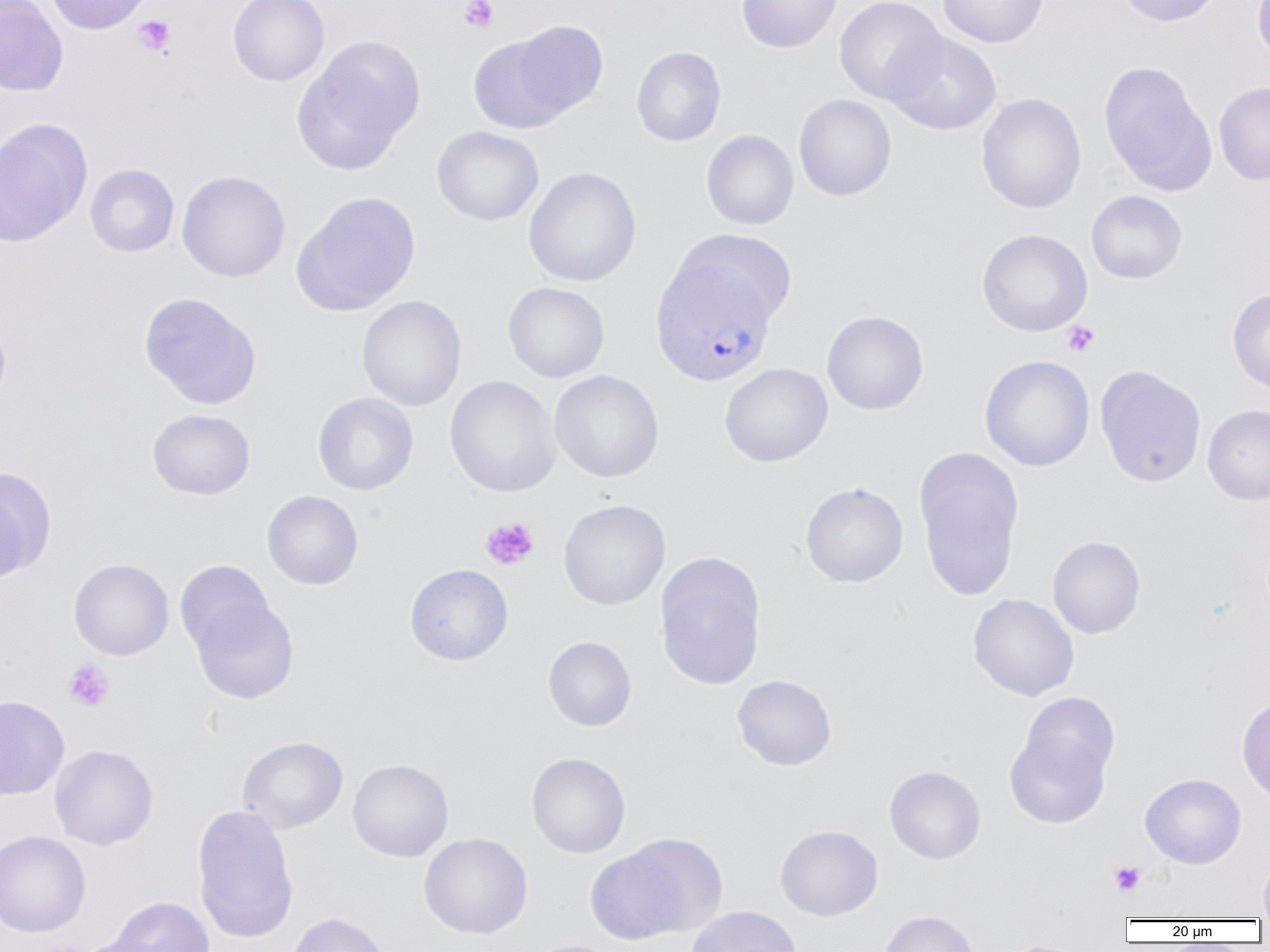
Summary:
  - Coordinate format: approximate bounding boxes as [x1, y1, x2, y2] in pixels
  - Plasmodium vivax-infected red blood cell locations: [650, 257, 777, 386]
  - Platelet locations: [459, 0, 499, 33], [133, 15, 175, 55], [1062, 320, 1099, 356], [480, 517, 539, 570], [63, 658, 115, 712], [1109, 860, 1145, 896]
  - Uninfected red blood cell locations: [0, 0, 69, 96], [43, 0, 152, 35], [228, 0, 330, 86], [736, 0, 842, 53], [834, 0, 947, 104], [937, 0, 1049, 48], [1116, 0, 1223, 27], [1252, 0, 1270, 65], [505, 20, 610, 121], [885, 31, 1001, 135], [468, 32, 577, 135], [293, 36, 425, 172], [631, 46, 726, 146], [1099, 62, 1216, 194], [1214, 80, 1270, 185], [976, 93, 1086, 214], [794, 94, 896, 201], [0, 117, 92, 247], [432, 126, 544, 226], [701, 129, 799, 230], [85, 164, 179, 257], [523, 167, 641, 287], [177, 170, 291, 282], [1086, 190, 1187, 284], [292, 191, 422, 316], [977, 228, 1092, 336], [674, 229, 798, 326], [503, 282, 610, 383], [1227, 288, 1270, 395], [138, 292, 262, 409], [356, 295, 466, 411], [822, 310, 929, 415], [0, 318, 11, 410], [979, 355, 1095, 472], [719, 363, 833, 467], [1095, 365, 1206, 487], [549, 370, 664, 482], [445, 375, 561, 497], [312, 392, 419, 495], [1203, 405, 1270, 505], [147, 409, 256, 500], [913, 446, 1025, 600], [0, 468, 55, 584], [800, 482, 908, 587], [261, 490, 363, 590], [558, 499, 670, 610], [1048, 536, 1146, 638], [654, 556, 766, 690], [69, 558, 174, 660], [175, 559, 276, 660], [404, 563, 513, 665], [968, 593, 1079, 701], [188, 595, 299, 704], [543, 636, 636, 731], [732, 674, 837, 771], [1019, 691, 1119, 783], [0, 695, 69, 800], [1237, 695, 1270, 804], [1004, 726, 1112, 830], [237, 736, 348, 834], [49, 744, 158, 850], [526, 752, 631, 858], [347, 759, 454, 862], [884, 765, 986, 864], [1140, 773, 1246, 869], [192, 803, 299, 944], [774, 824, 883, 920], [0, 830, 90, 938], [418, 832, 533, 939], [591, 835, 725, 941], [1258, 849, 1270, 919], [106, 896, 215, 952], [685, 906, 802, 952], [878, 910, 980, 952], [286, 912, 391, 952], [71, 936, 167, 952], [1000, 938, 1095, 952], [523, 939, 628, 952]
  - Slide-level diagnosis: Plasmodium vivax
  - Image size: 1270×952 pixels
  - Magnification: 1000x
  - Modality: light microscopy
  - Field of view: single
  - Preparation: thin blood smear